Assess the morphology of the erythrocytes.
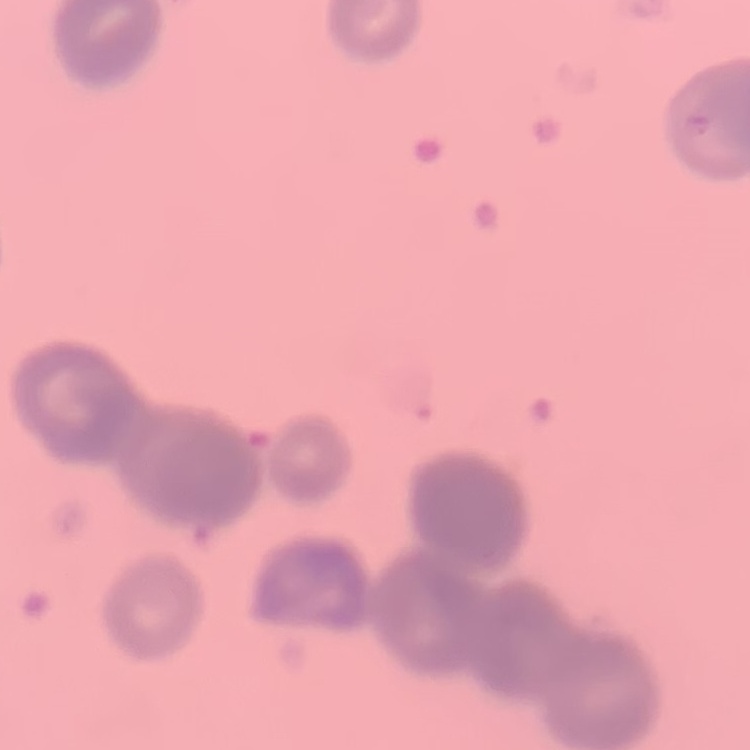

They show rouleaux formation.

preparation = thin blood smear
stain = Field's or Giemsa
image type = one tile cut from a larger photomicrograph